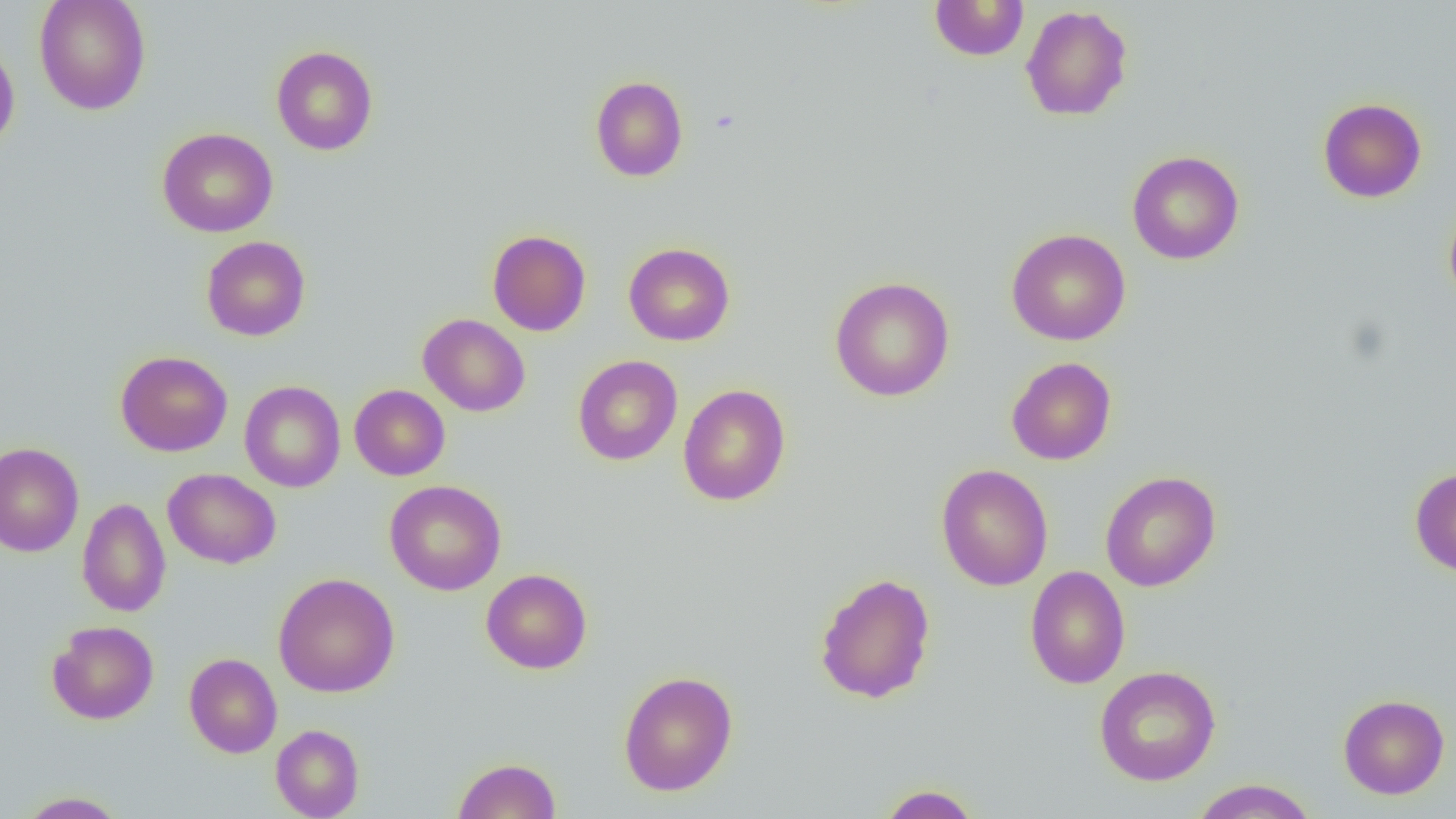
slide-level diagnosis = no evidence of blood parasites
modality = optical microscopy
uninfected red blood cell locations = approximate bounding boxes as named x1/y1/x2/y2 corners in pixels: (x1=34, y1=0, x2=151, y2=115), (x1=929, y1=0, x2=1029, y2=61), (x1=1021, y1=5, x2=1132, y2=121), (x1=0, y1=38, x2=20, y2=153), (x1=271, y1=45, x2=378, y2=155), (x1=590, y1=75, x2=688, y2=182), (x1=1318, y1=97, x2=1427, y2=203), (x1=157, y1=127, x2=278, y2=237), (x1=1127, y1=150, x2=1244, y2=265), (x1=1444, y1=200, x2=1456, y2=309), (x1=1006, y1=229, x2=1131, y2=346), (x1=487, y1=230, x2=591, y2=336), (x1=201, y1=236, x2=311, y2=341), (x1=623, y1=242, x2=735, y2=346), (x1=829, y1=276, x2=954, y2=401), (x1=418, y1=313, x2=530, y2=417), (x1=116, y1=350, x2=232, y2=456), (x1=572, y1=355, x2=683, y2=466), (x1=1006, y1=357, x2=1116, y2=465), (x1=239, y1=380, x2=346, y2=492), (x1=678, y1=383, x2=791, y2=506), (x1=349, y1=384, x2=450, y2=481), (x1=0, y1=442, x2=84, y2=557), (x1=936, y1=463, x2=1053, y2=591), (x1=1410, y1=467, x2=1456, y2=577), (x1=163, y1=468, x2=281, y2=569), (x1=1100, y1=471, x2=1221, y2=591), (x1=384, y1=480, x2=506, y2=595), (x1=77, y1=498, x2=171, y2=617), (x1=1025, y1=566, x2=1131, y2=689), (x1=481, y1=568, x2=593, y2=674), (x1=814, y1=572, x2=936, y2=704), (x1=273, y1=573, x2=400, y2=697), (x1=47, y1=620, x2=159, y2=724), (x1=184, y1=653, x2=282, y2=758), (x1=1094, y1=665, x2=1221, y2=786), (x1=618, y1=670, x2=738, y2=796), (x1=1338, y1=694, x2=1450, y2=799), (x1=270, y1=724, x2=364, y2=818), (x1=453, y1=757, x2=561, y2=819), (x1=1190, y1=778, x2=1318, y2=818), (x1=876, y1=783, x2=983, y2=818), (x1=15, y1=791, x2=128, y2=818)
field of view = one of a larger specimen
image size = 1456×819 pixels
preparation = thin blood smear
magnification = 1000x